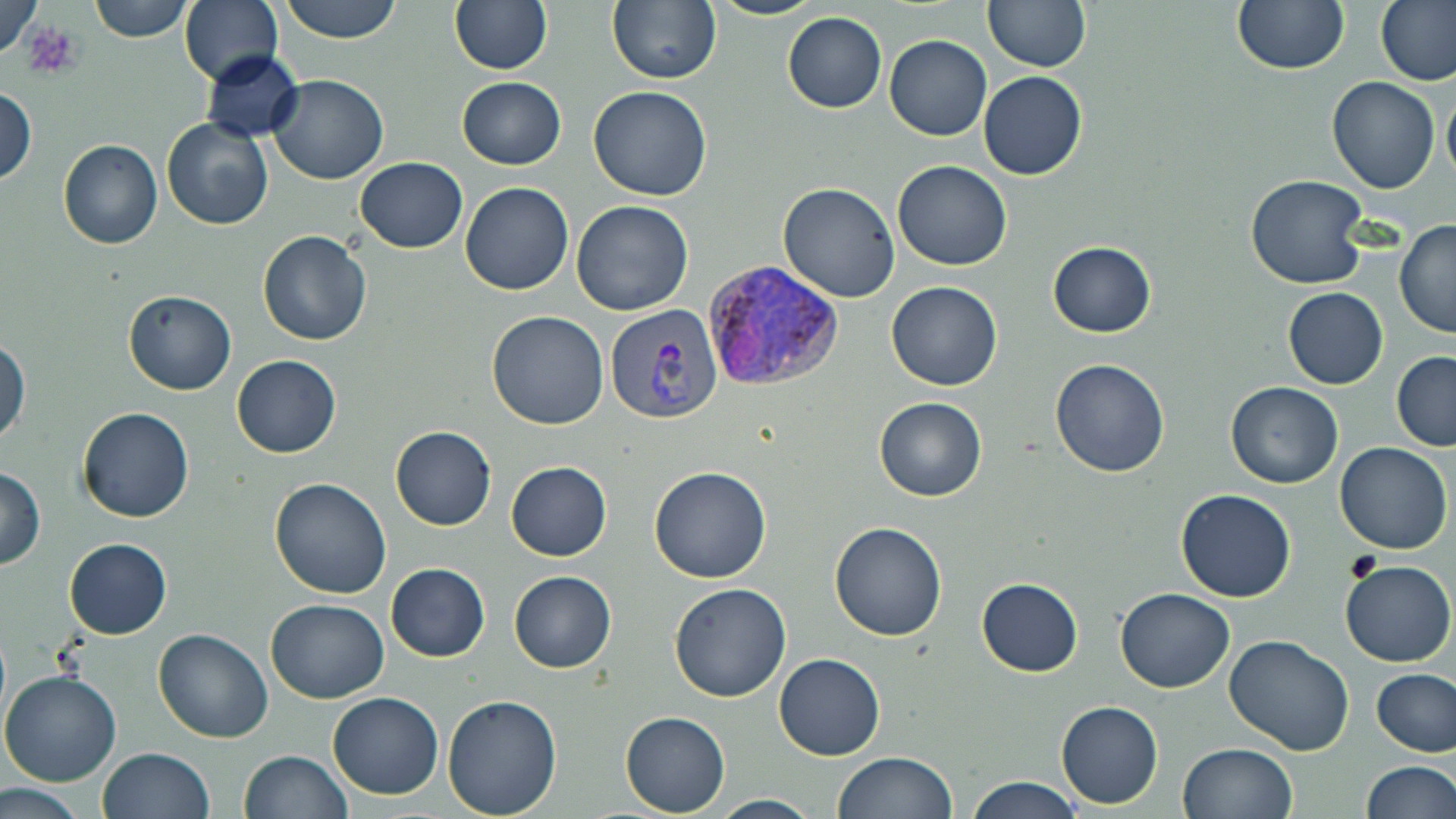

Summary:
  - Coordinate format: approximate bounding boxes as [x1, y1, x2, y2] in pixels
  - Platelet locations: [20, 21, 78, 75]
  - Uninfected red blood cell locations: [89, 0, 193, 42], [179, 0, 281, 87], [279, 0, 404, 45], [449, 0, 553, 75], [608, 0, 722, 87], [711, 0, 825, 21], [983, 0, 1089, 72], [1231, 0, 1347, 74], [1377, 0, 1456, 86], [0, 1, 45, 61], [783, 11, 886, 112], [885, 35, 992, 141], [201, 49, 303, 143], [979, 71, 1087, 180], [267, 75, 389, 185], [457, 76, 566, 169], [1327, 76, 1440, 194], [1443, 81, 1456, 189], [589, 85, 711, 203], [0, 86, 36, 187], [162, 117, 274, 231], [59, 138, 163, 250], [354, 157, 469, 252], [893, 161, 1011, 270], [1245, 174, 1370, 290], [459, 181, 574, 295], [776, 182, 902, 303], [572, 200, 693, 316], [1394, 217, 1456, 340], [257, 230, 372, 345], [1047, 241, 1156, 338], [884, 281, 1003, 390], [1282, 287, 1388, 389], [122, 289, 236, 394], [486, 310, 608, 430], [0, 337, 29, 448], [1391, 352, 1456, 451], [231, 354, 342, 458], [1049, 358, 1172, 477], [1226, 381, 1343, 488], [874, 397, 987, 501], [77, 407, 195, 523], [390, 426, 496, 531], [1334, 442, 1452, 554], [506, 461, 612, 560], [1, 465, 45, 570], [649, 465, 774, 583], [268, 476, 392, 599], [1175, 490, 1296, 603], [830, 522, 947, 642], [63, 537, 172, 639], [1341, 560, 1455, 668], [386, 563, 490, 661], [508, 571, 616, 673], [977, 577, 1083, 676], [669, 582, 791, 703], [1115, 588, 1235, 692], [265, 599, 390, 703], [152, 629, 274, 744], [1224, 636, 1354, 755], [775, 653, 886, 760], [1372, 669, 1455, 755], [0, 670, 122, 787], [327, 692, 444, 799], [442, 694, 563, 817], [1055, 701, 1163, 810], [619, 711, 730, 817], [1177, 743, 1297, 819], [97, 747, 215, 819], [238, 749, 353, 819], [833, 751, 958, 819], [1358, 760, 1454, 819], [967, 777, 1085, 817], [1, 783, 92, 817], [707, 794, 820, 818]
  - Plasmodium vivax-infected red blood cell locations: [703, 260, 844, 396], [605, 304, 722, 422]
  - Slide-level diagnosis: Plasmodium vivax
  - Preparation: thin blood film
  - Field of view: one of a larger specimen
  - Image size: 1456×819 pixels
  - Magnification: 1000x
  - Modality: optical microscopy
  - Stain: May-Grünwald-Giemsa